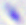

modality = photomicrograph
identification = Toxoplasma gondii
magnification = 400x